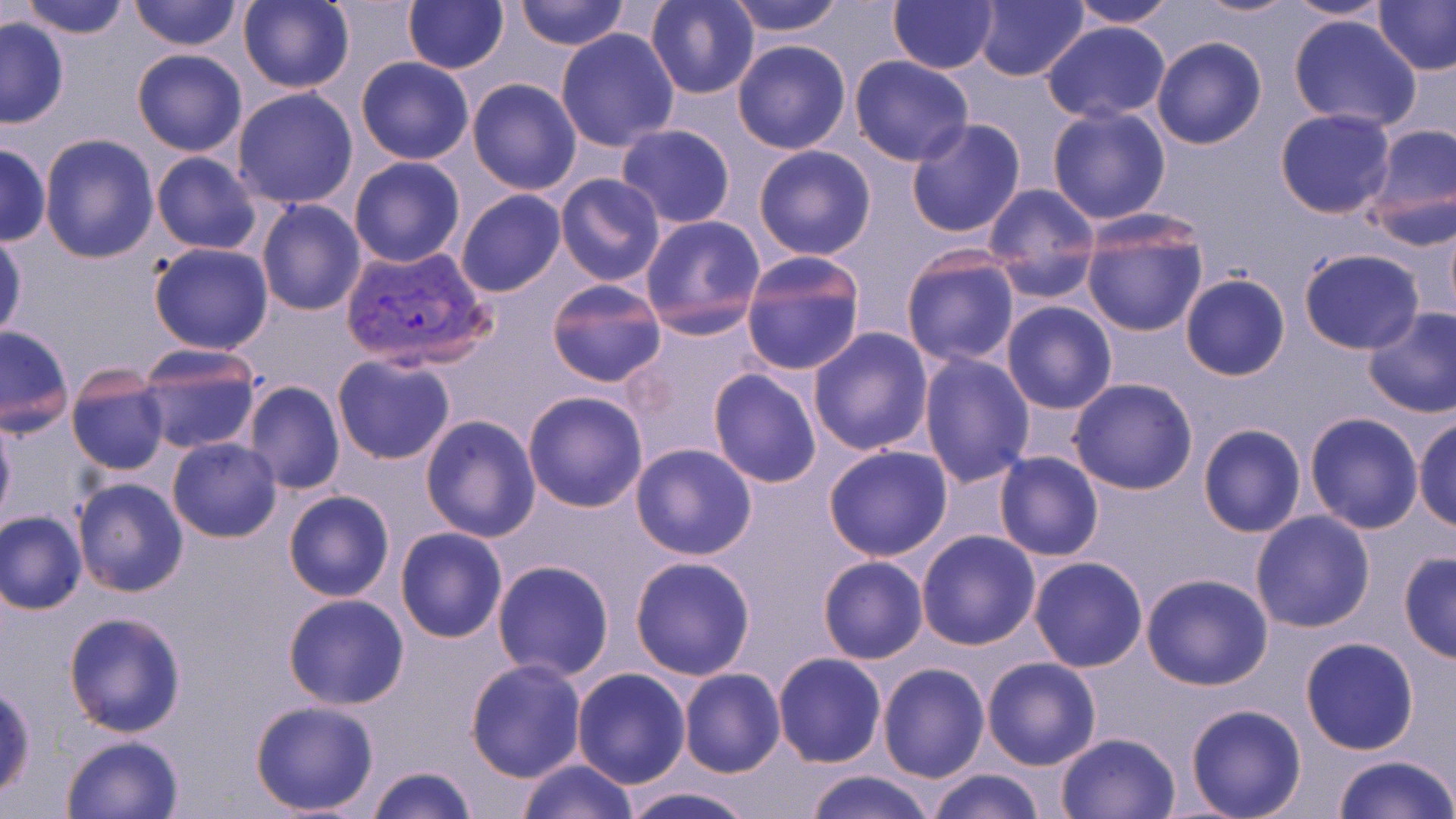

Summary:
  - Coordinate format: approximate bounding boxes as (x1,y1)-(x2,y2) corner pairs in pixels
  - Plasmodium vivax-infected red blood cell locations: (340,244)-(492,371)
  - Uninfected red blood cell locations: (19,0)-(131,40), (127,0)-(241,49), (402,0)-(508,74), (512,0)-(628,52), (726,0)-(845,36), (887,0)-(998,74), (973,0)-(1089,84), (1065,0)-(1178,27), (1191,0)-(1302,19), (1281,0)-(1392,23), (1371,0)-(1456,75), (239,1)-(355,94), (645,1)-(762,100), (1288,15)-(1423,132), (0,16)-(70,128), (1041,21)-(1169,124), (555,28)-(680,152), (1150,36)-(1267,150), (731,38)-(852,154), (132,49)-(248,157), (498,54)-(672,180), (848,55)-(975,167), (356,57)-(473,165), (465,78)-(582,195), (231,87)-(360,209), (1046,105)-(1173,224), (1274,108)-(1397,219), (905,116)-(1028,238), (615,123)-(735,229), (1364,123)-(1455,242), (39,134)-(159,264), (0,143)-(50,247), (752,144)-(876,260), (151,151)-(263,255), (349,157)-(465,268), (554,173)-(666,289), (982,183)-(1100,298), (456,190)-(566,297), (256,200)-(367,316), (1080,214)-(1210,338), (639,215)-(766,338), (1,231)-(26,343), (148,242)-(273,353), (1298,248)-(1425,354), (901,250)-(1021,368), (739,252)-(866,376), (1180,275)-(1289,382), (545,279)-(668,389), (1001,302)-(1116,414), (1362,306)-(1456,419), (623,316)-(765,455), (0,326)-(74,437), (808,328)-(934,455), (133,345)-(264,456), (917,350)-(1035,488), (331,355)-(455,465), (66,364)-(170,476), (707,369)-(822,489), (1069,377)-(1198,495), (242,381)-(345,495), (522,390)-(650,512), (1303,412)-(1424,533), (420,414)-(543,541), (0,415)-(15,528), (1412,416)-(1456,531), (1197,423)-(1306,537), (167,436)-(282,542), (630,442)-(758,561), (823,445)-(953,562), (994,451)-(1105,562), (73,476)-(189,598), (283,489)-(395,602), (1,510)-(87,614), (1250,510)-(1376,633), (395,528)-(507,643), (915,530)-(1041,650), (1398,552)-(1456,664), (629,555)-(757,680), (817,556)-(927,664), (1027,556)-(1148,673), (491,559)-(616,682), (1140,573)-(1273,692), (283,593)-(411,710), (62,609)-(188,737), (1300,637)-(1418,755), (772,652)-(887,768), (981,657)-(1103,771), (465,659)-(587,782), (877,663)-(990,784), (571,667)-(691,789), (678,668)-(786,778), (0,679)-(36,805), (247,699)-(380,816), (1184,703)-(1308,819), (1054,731)-(1181,818), (60,734)-(186,819), (1330,754)-(1456,819), (514,757)-(637,819), (365,765)-(476,819), (928,768)-(1046,819), (805,769)-(938,819), (615,785)-(759,819)
  - Slide-level diagnosis: Plasmodium vivax
  - Magnification: 1000x
  - Field of view: one of a larger specimen
  - Preparation: thin blood film
  - Modality: optical microscopy
  - Stain: May-Grünwald-Giemsa
  - Image size: 1456×819 pixels